Point out leukocytes.
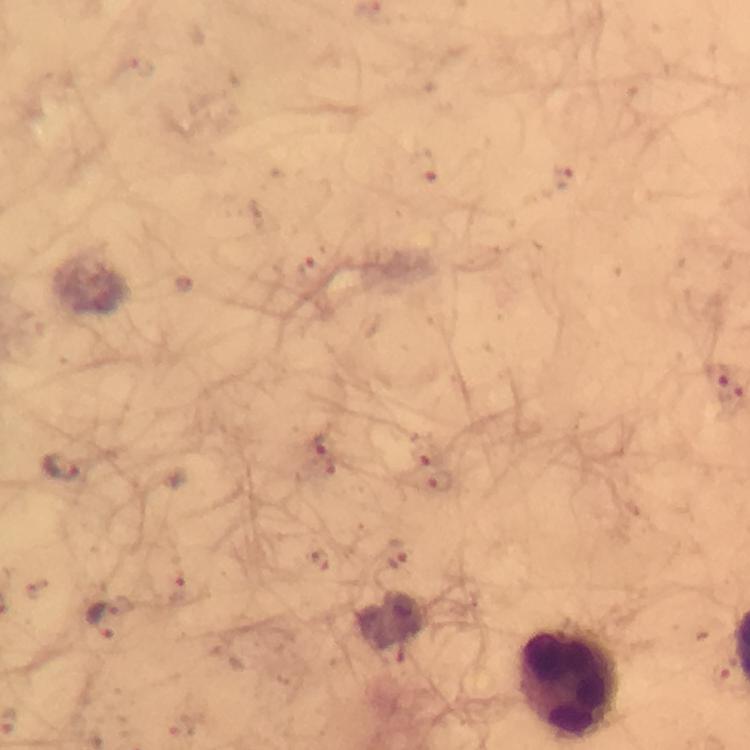
Approximate centers as {x, y} in pixels.
Leukocytes: {569, 684}.

{
  "stain": "Giemsa",
  "cropped_from": "a single field of view",
  "magnification": "100x",
  "preparation": "thick blood film",
  "immersion_oil": "applied",
  "malaria_parasite_locations": "approximate centers as {x, y} in pixels: {423, 165}, {563, 178}, {719, 372}, {731, 394}, {319, 444}, {426, 455}, {64, 467}, {440, 482}, {396, 553}, {105, 619}",
  "image_size": "750×750 pixels",
  "capture": "smartphone camera through the microscope",
  "context": "from a malaria diagnostic workup"
}